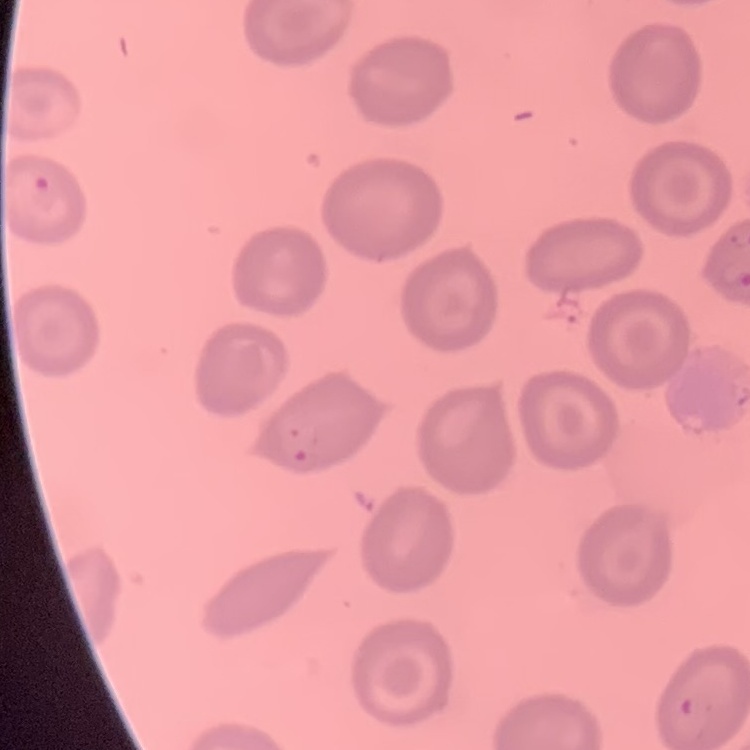

The red blood cells exhibit no rouleaux formation. One tile cut from a larger photomicrograph. Stained with either Field's or Giemsa. Thin peripheral smear.